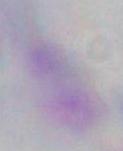
Summary:
  - Magnification: 1000x
  - Modality: photomicrograph
  - Identification: Toxoplasma gondii